Identify the parasite.
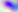

This is Toxoplasma gondii.

400x magnification. Photomicrograph.